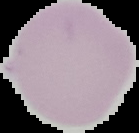
Summary:
  - Image type: cell region segmented out of the field of view; surrounding area masked to black
  - Preparation: thin blood smear
  - Malaria status: uninfected
  - Image size: 139×133 pixels